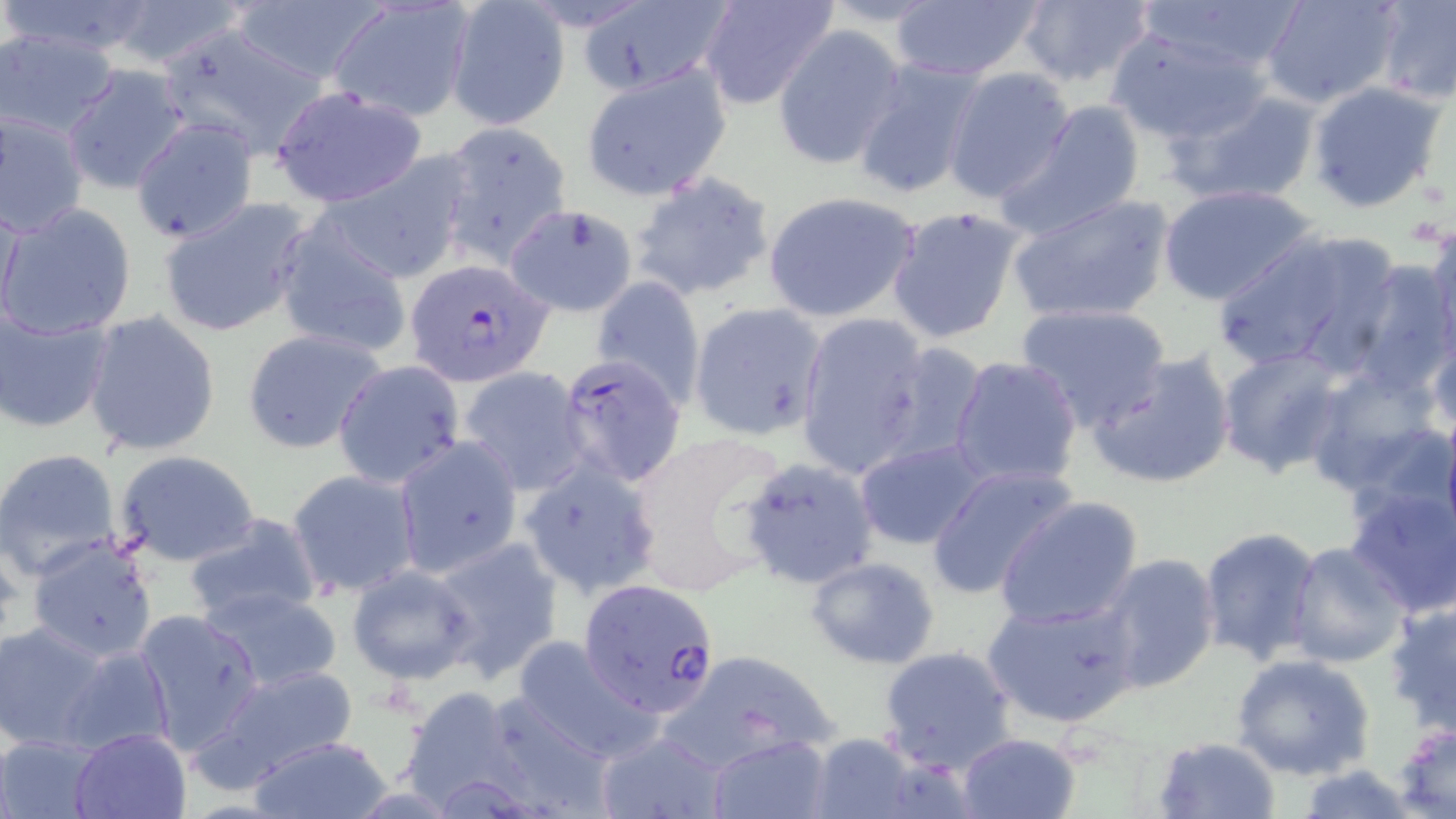 Approximate bounding boxes as (x1,y1)-(x2,y2) corner pairs in pixels. Uninfected red blood cell locations: (3,0)-(169,62), (98,0)-(250,71), (226,0)-(386,85), (444,0)-(573,129), (1014,0)-(1157,92), (1135,0)-(1304,82), (1260,0)-(1403,108), (1375,0)-(1456,103), (887,1)-(1045,82), (696,2)-(842,110), (327,3)-(472,122), (153,24)-(329,158), (772,24)-(908,170), (1106,27)-(1274,145), (1,29)-(122,139), (849,57)-(988,199), (61,64)-(192,195), (580,64)-(732,201), (942,67)-(1075,204), (1305,82)-(1447,215), (272,87)-(431,206), (1169,87)-(1322,207), (1000,101)-(1146,238), (2,107)-(88,240), (436,121)-(573,266), (316,155)-(472,283), (629,170)-(780,305), (1157,184)-(1321,305), (761,189)-(922,322), (1005,191)-(1176,325), (1,195)-(22,336), (157,196)-(314,338), (515,200)-(649,310), (2,202)-(137,340), (885,205)-(1026,345), (272,219)-(413,360), (1426,221)-(1456,359), (1213,228)-(1400,379), (1342,260)-(1456,395), (592,276)-(706,404), (688,301)-(829,441), (1014,301)-(1171,430), (0,306)-(114,434), (82,311)-(222,458), (795,313)-(929,476), (1428,323)-(1456,445), (242,329)-(389,455), (875,341)-(991,467), (1215,346)-(1350,477), (1088,352)-(1236,490), (950,356)-(1083,491), (333,360)-(464,487), (1304,361)-(1452,506), (459,368)-(590,494), (1439,406)-(1456,542), (630,429)-(793,586), (393,437)-(525,577), (851,439)-(991,549), (0,447)-(123,579), (113,450)-(263,567), (737,457)-(883,593), (518,461)-(662,599), (926,464)-(1078,600), (288,469)-(421,599), (1342,482)-(1456,619), (993,495)-(1144,631), (182,512)-(326,629), (1198,526)-(1324,665), (25,535)-(161,665), (430,536)-(563,681), (1282,542)-(1408,670), (1094,553)-(1221,695), (805,555)-(941,670), (345,565)-(480,685), (199,587)-(345,691), (981,596)-(1141,729), (1385,600)-(1456,738), (133,609)-(265,754), (0,622)-(114,753), (509,637)-(659,761), (57,643)-(176,758), (879,646)-(1016,773), (658,648)-(841,772), (1229,653)-(1376,782), (199,663)-(360,795), (394,685)-(540,814), (473,689)-(616,817), (1391,721)-(1455,817), (70,727)-(190,818), (594,729)-(729,819), (800,731)-(938,819), (1,733)-(105,817), (954,733)-(1082,819), (246,734)-(395,818), (706,734)-(832,819), (1152,736)-(1280,819). Plasmodium falciparum-infected red blood cell locations: (405,259)-(554,386), (557,352)-(686,487), (578,576)-(719,716). Slide-level diagnosis: Plasmodium falciparum. Image is 1456×819 pixels. Thin blood smear. May-Grünwald-Giemsa-stained preparation. Captured at 1000x magnification. One field of a larger specimen. Light microscopy.